Outline each blood parasite and name the species.
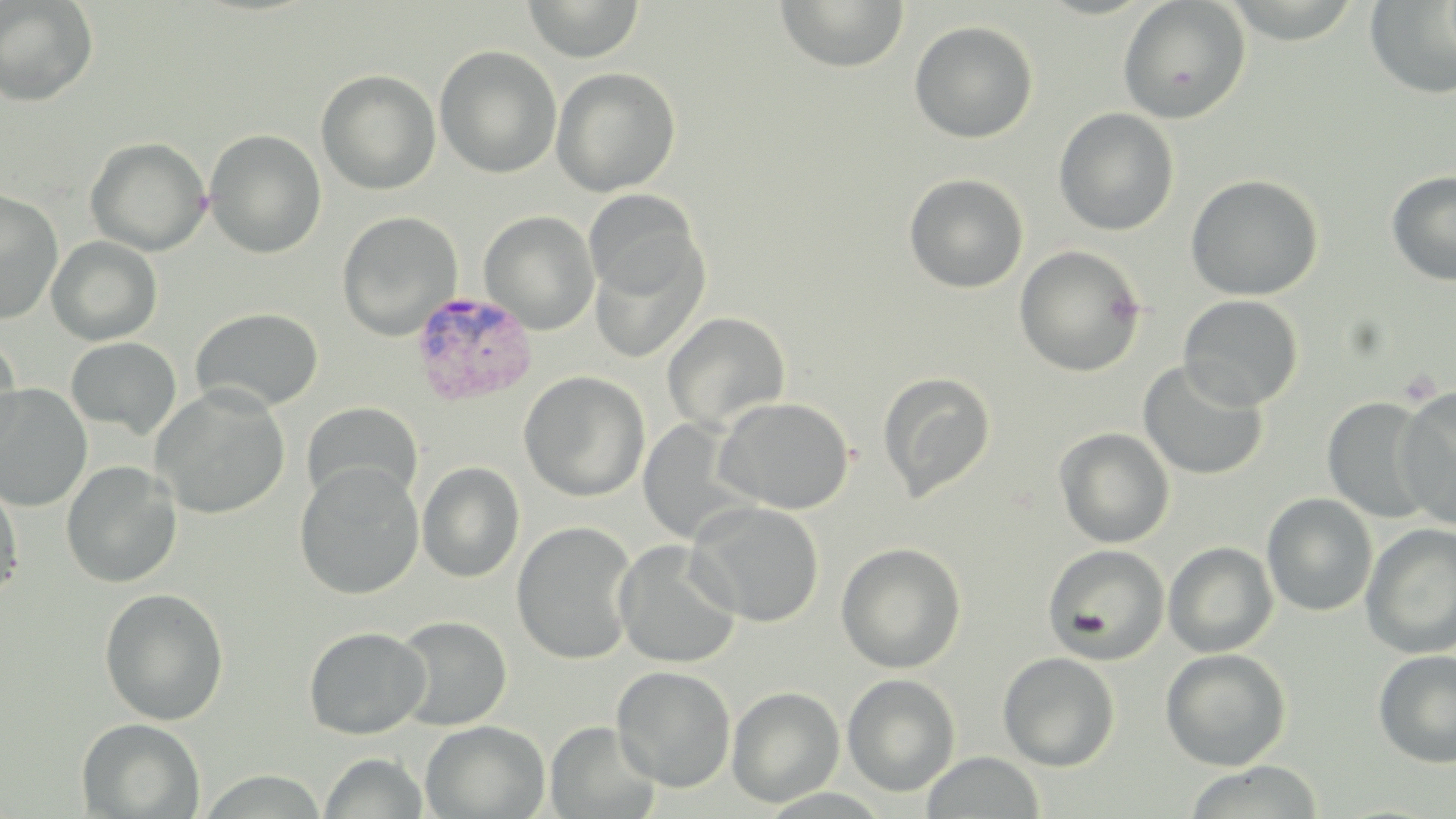
Approximate bounding boxes as (x1,y1)-(x2,y2) corner pairs in pixels.
Plasmodium vivax-infected red blood cells: (410,289)-(537,406).
No Plasmodium falciparum, Plasmodium ovale, Plasmodium malariae, Babesia divergens, or Trypanosoma brucei observed.

Summary:
  - Uninfected red blood cell locations: (0,0)-(98,106), (523,0)-(644,62), (775,0)-(910,74), (1117,0)-(1251,124), (1364,2)-(1456,100), (909,20)-(1038,143), (434,46)-(562,179), (551,67)-(681,197), (316,69)-(441,194), (1054,108)-(1179,236), (204,129)-(326,258), (85,137)-(211,256), (1385,169)-(1456,286), (903,173)-(1029,293), (1185,174)-(1323,301), (0,189)-(64,324), (583,190)-(703,301), (479,210)-(600,334), (337,211)-(462,341), (589,233)-(709,363), (46,236)-(163,346), (1014,245)-(1147,378), (1178,294)-(1303,410), (189,307)-(324,413), (662,311)-(791,433), (0,334)-(23,457), (66,337)-(182,438), (1138,359)-(1270,480), (518,371)-(651,502), (877,371)-(996,502), (0,383)-(93,511), (151,386)-(291,519), (1395,387)-(1456,529), (714,396)-(854,514), (1322,396)-(1436,525), (301,401)-(423,508), (637,419)-(750,544), (1054,427)-(1175,548), (60,460)-(182,589), (417,461)-(525,583), (294,462)-(425,599), (0,480)-(24,604), (1262,493)-(1377,617), (687,501)-(825,627), (512,521)-(638,665), (1361,524)-(1456,658), (613,540)-(741,669), (836,541)-(967,673), (1163,541)-(1278,658), (1043,544)-(1170,665), (98,586)-(230,725), (392,615)-(512,731), (303,626)-(430,740), (1160,648)-(1292,771), (1372,649)-(1456,767), (998,652)-(1120,771), (611,665)-(736,792), (842,673)-(960,796), (726,686)-(845,807), (76,717)-(205,818), (420,720)-(550,819), (545,721)-(662,818), (922,751)-(1045,818), (320,752)-(428,818), (1182,761)-(1325,819)
  - Slide-level diagnosis: Plasmodium vivax
  - Magnification: 1000x
  - Modality: light microscopy
  - Stain: May-Grünwald-Giemsa
  - Preparation: thin blood smear
  - Image size: 1456×819 pixels
  - Field of view: one of a larger specimen